Report the malaria status of this cell.
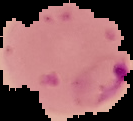
Parasitized.

Summary:
  - Image type: cell region segmented out of the field of view; surrounding area masked to black
  - Preparation: thin blood film
  - Image size: 133×121 pixels